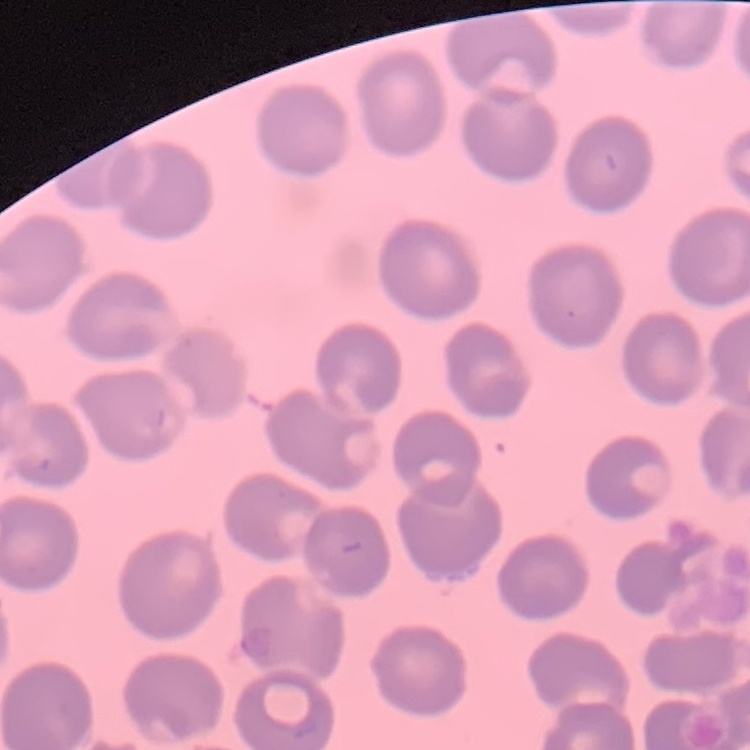
The erythrocytes show no rouleaux formation. One tile cut from a larger photomicrograph. Field's or Giemsa stain. Thin blood film.